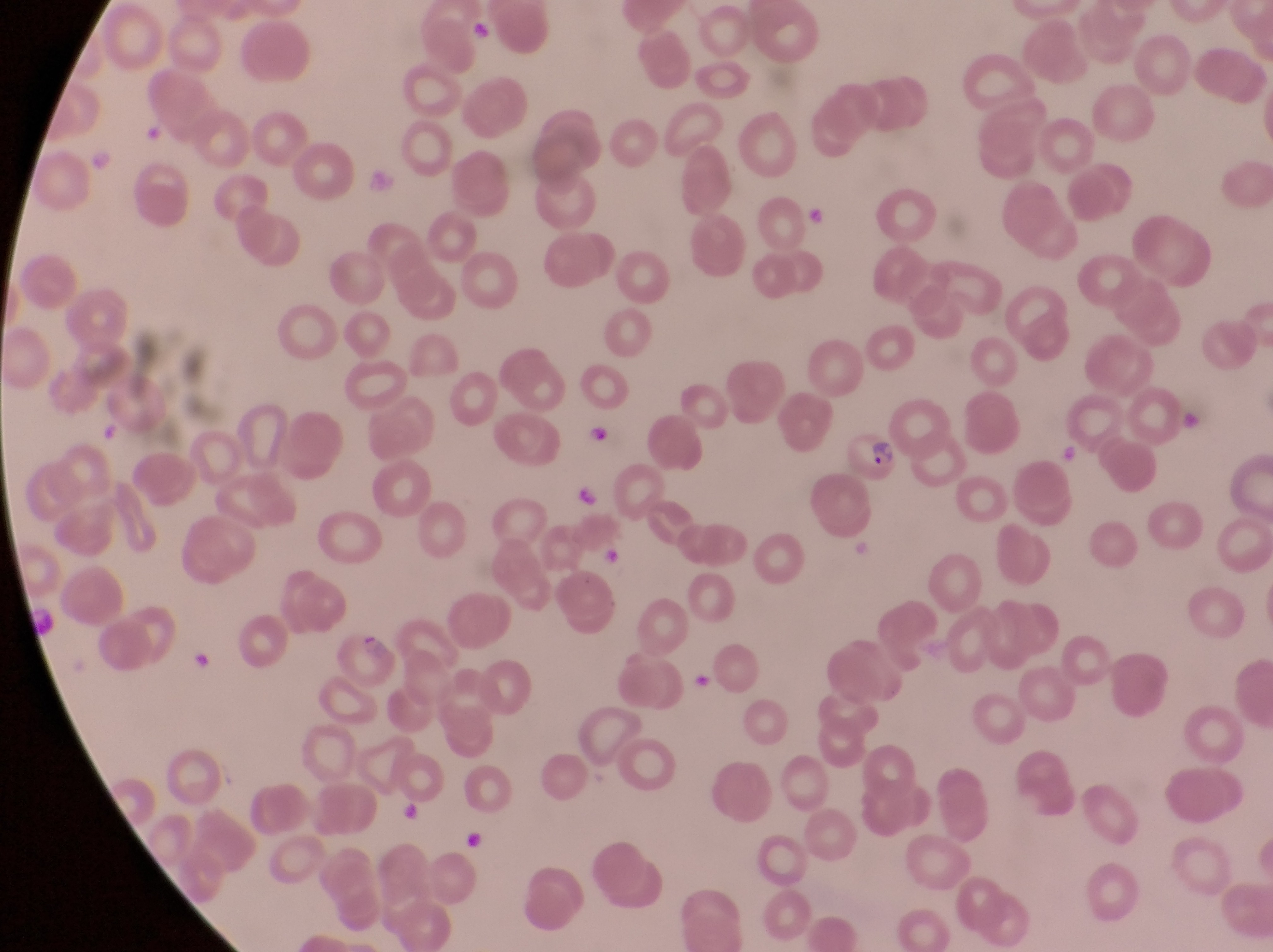

Approximate bounding boxes as {left, top, right, bottom} in pixels. Artifact (platelet-like body, stain precipitate, or debris) locations: {473, 15, 494, 46}, {804, 206, 830, 230}, {590, 423, 614, 449}, {572, 482, 598, 503}, {601, 544, 624, 568}, {692, 669, 715, 695}, {399, 804, 422, 827}, {462, 830, 494, 862}. Parasitised red blood cell locations: {834, 422, 903, 485}, {335, 626, 402, 698}. Photographed through the eyepiece of an Olympus CX-23 microscope with a smartphone camera. Image is 1273×952 pixels. Thin blood film. One field of view. Magnification of 1000x. Sample from Uganda.